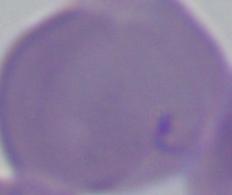
Summary:
  - Modality: photomicrograph
  - Magnification: 1000x
  - Identification: Babesia